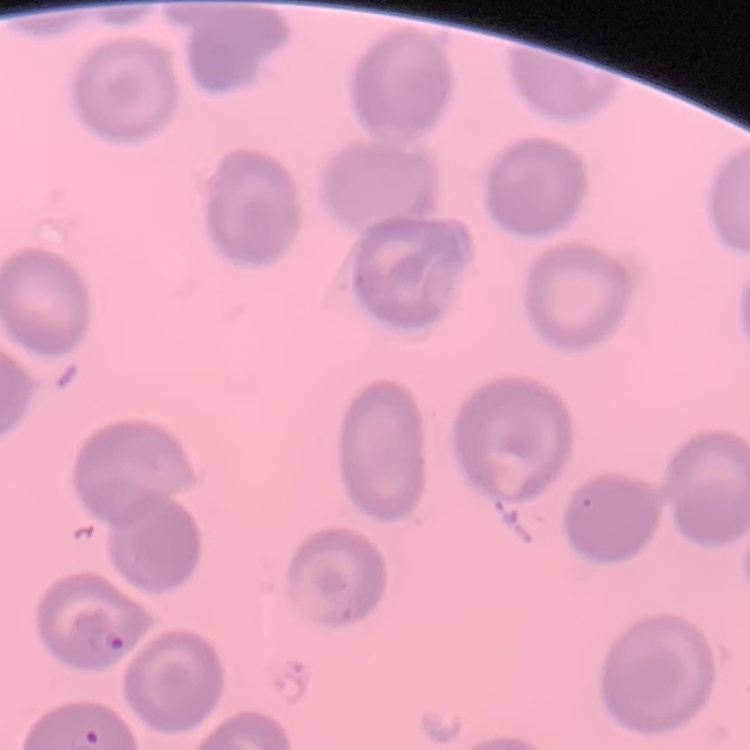

{
  "erythrocyte_morphology": "no rouleaux formation",
  "stain": "Field's or Giemsa",
  "image_type": "one tile cut from a larger photomicrograph",
  "preparation": "thin peripheral smear"
}